Report the malaria status of this cell.
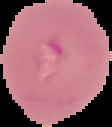

Uninfected.

The area outside the segmented cell region is set to black. Image is 112×127 pixels. From a thin blood smear.